Assess the morphology of the erythrocytes.
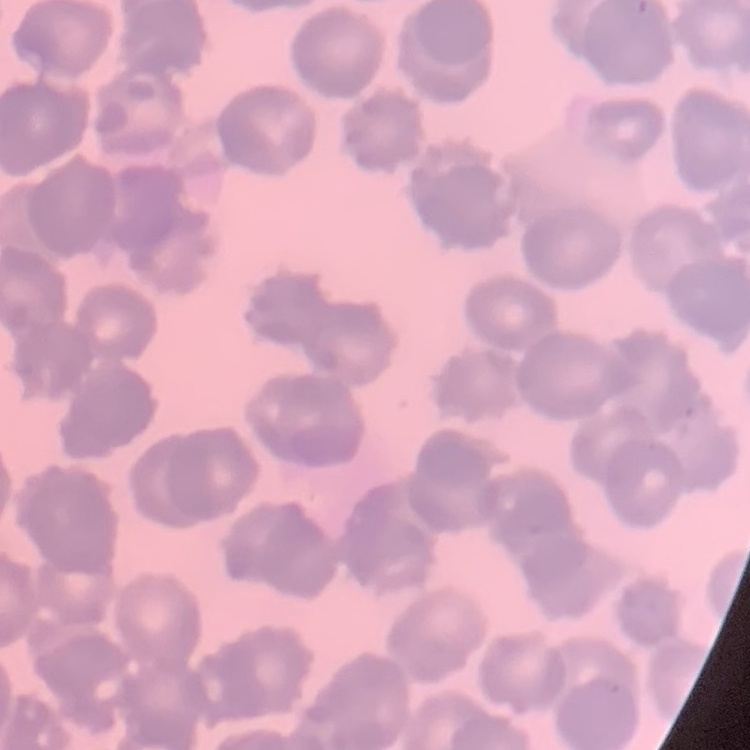
Rouleaux formation.

{
  "stain": "Field's or Giemsa",
  "preparation": "thin peripheral smear",
  "image_type": "square crop of a larger photomicrograph"
}